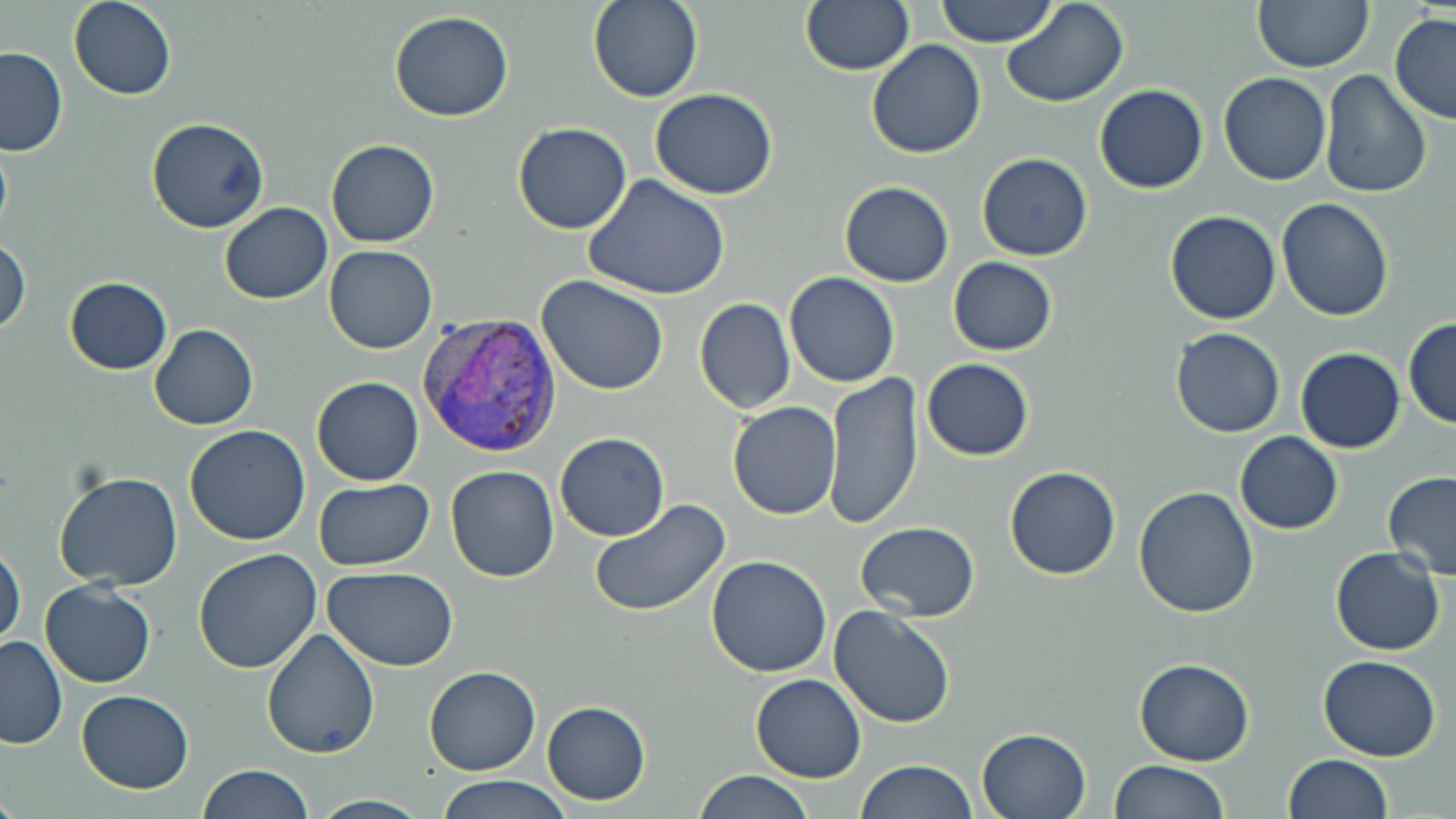

Summary:
  - Coordinate format: approximate bounding boxes as [x1, y1, x2, y2] in pixels
  - Plasmodium vivax-infected red blood cell locations: [419, 312, 562, 458]
  - Uninfected red blood cell locations: [68, 0, 177, 101], [588, 0, 704, 104], [800, 0, 913, 75], [934, 0, 1059, 47], [1252, 0, 1373, 72], [1001, 1, 1130, 109], [389, 11, 515, 121], [1389, 14, 1456, 125], [867, 39, 986, 160], [0, 47, 69, 157], [1319, 69, 1432, 197], [1219, 73, 1330, 186], [1094, 84, 1208, 194], [650, 89, 778, 199], [147, 117, 271, 234], [513, 122, 633, 234], [0, 131, 13, 247], [326, 139, 439, 247], [977, 152, 1093, 261], [585, 176, 731, 300], [839, 181, 954, 287], [1277, 198, 1394, 321], [219, 203, 333, 304], [1165, 210, 1281, 325], [1, 237, 31, 339], [323, 245, 438, 354], [948, 257, 1058, 355], [784, 271, 900, 388], [536, 275, 670, 395], [64, 277, 172, 374], [693, 297, 796, 415], [1402, 317, 1456, 429], [149, 324, 258, 430], [1170, 327, 1286, 437], [1296, 348, 1405, 453], [921, 358, 1035, 462], [820, 371, 925, 533], [312, 376, 423, 486], [728, 400, 841, 520], [185, 426, 311, 546], [1235, 431, 1343, 534], [555, 433, 670, 541], [445, 466, 560, 582], [1005, 467, 1121, 580], [54, 471, 185, 590], [1382, 472, 1456, 581], [312, 480, 435, 571], [1132, 484, 1259, 618], [589, 498, 732, 618], [855, 522, 980, 620], [1, 543, 27, 648], [1330, 547, 1444, 656], [192, 548, 322, 674], [705, 555, 833, 677], [322, 567, 459, 671], [40, 580, 157, 688], [829, 605, 955, 728], [262, 627, 381, 759], [0, 635, 67, 748], [1317, 654, 1441, 761], [1134, 658, 1255, 766], [424, 666, 540, 775], [750, 673, 866, 783], [78, 690, 193, 793], [542, 701, 651, 804], [977, 728, 1091, 818], [1283, 754, 1393, 818], [856, 759, 979, 819], [1111, 759, 1228, 818], [197, 765, 314, 819], [692, 770, 815, 819], [436, 775, 573, 818]
  - Slide-level diagnosis: Plasmodium vivax
  - Field of view: one of a larger specimen
  - Magnification: 1000x
  - Stain: May-Grünwald-Giemsa
  - Modality: optical microscopy
  - Image size: 1456×819 pixels
  - Preparation: thin blood film